Report the malaria status of this cell.
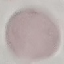
It is uninfected.

Summary:
  - Image type: cell patch, automatically extracted from a larger field of view and resized to 64 × 64 pixels
  - Capture: smartphone through the microscope eyepiece
  - Preparation: thin blood film
  - Stain: Giemsa